Assess this cell for malaria.
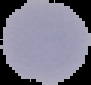
It is uninfected.

From a thin blood smear. Image is 91×85 pixels. The area outside the segmented cell region is set to black.